Assess the morphology of the erythrocytes.
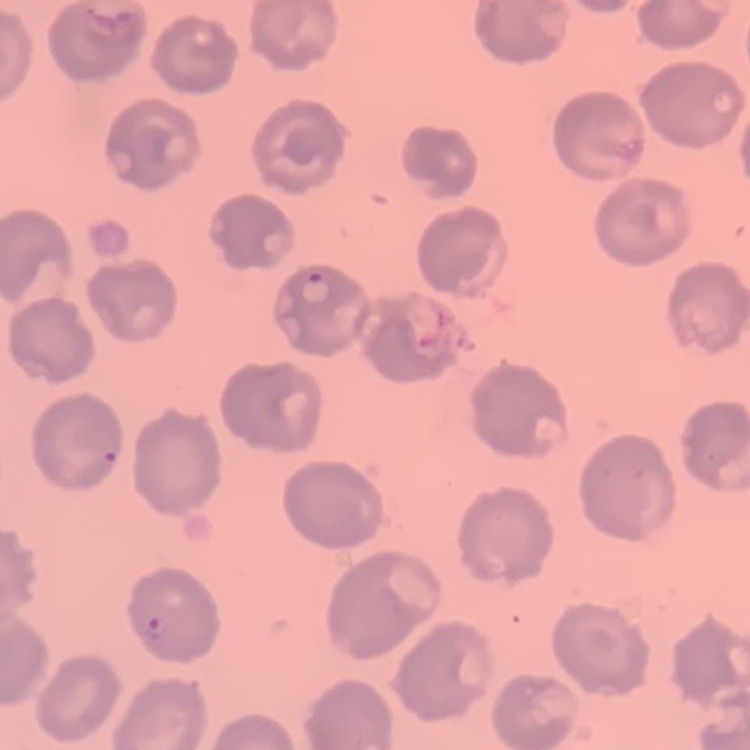
No rouleaux formation.

Summary:
  - Preparation: thin peripheral smear
  - Stain: Field's or Giemsa
  - Image type: one tile cut from a larger photomicrograph